Assess the morphology of the red blood cells.
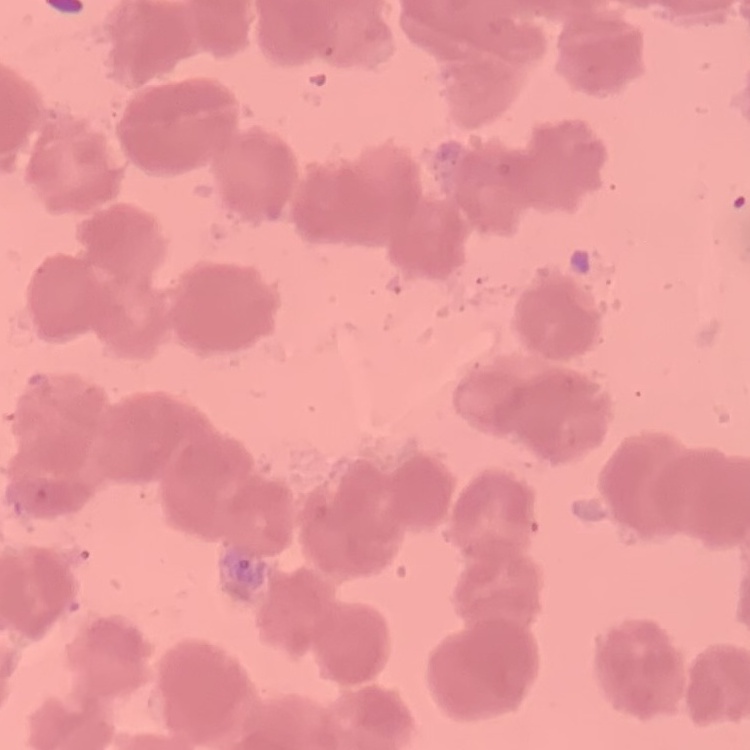

Rouleaux formation.

Field's or Giemsa stain. Square crop of a larger photomicrograph. Thin peripheral smear.